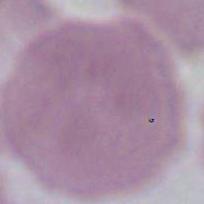

identification = red blood cell
modality = micrograph
magnification = 1000x